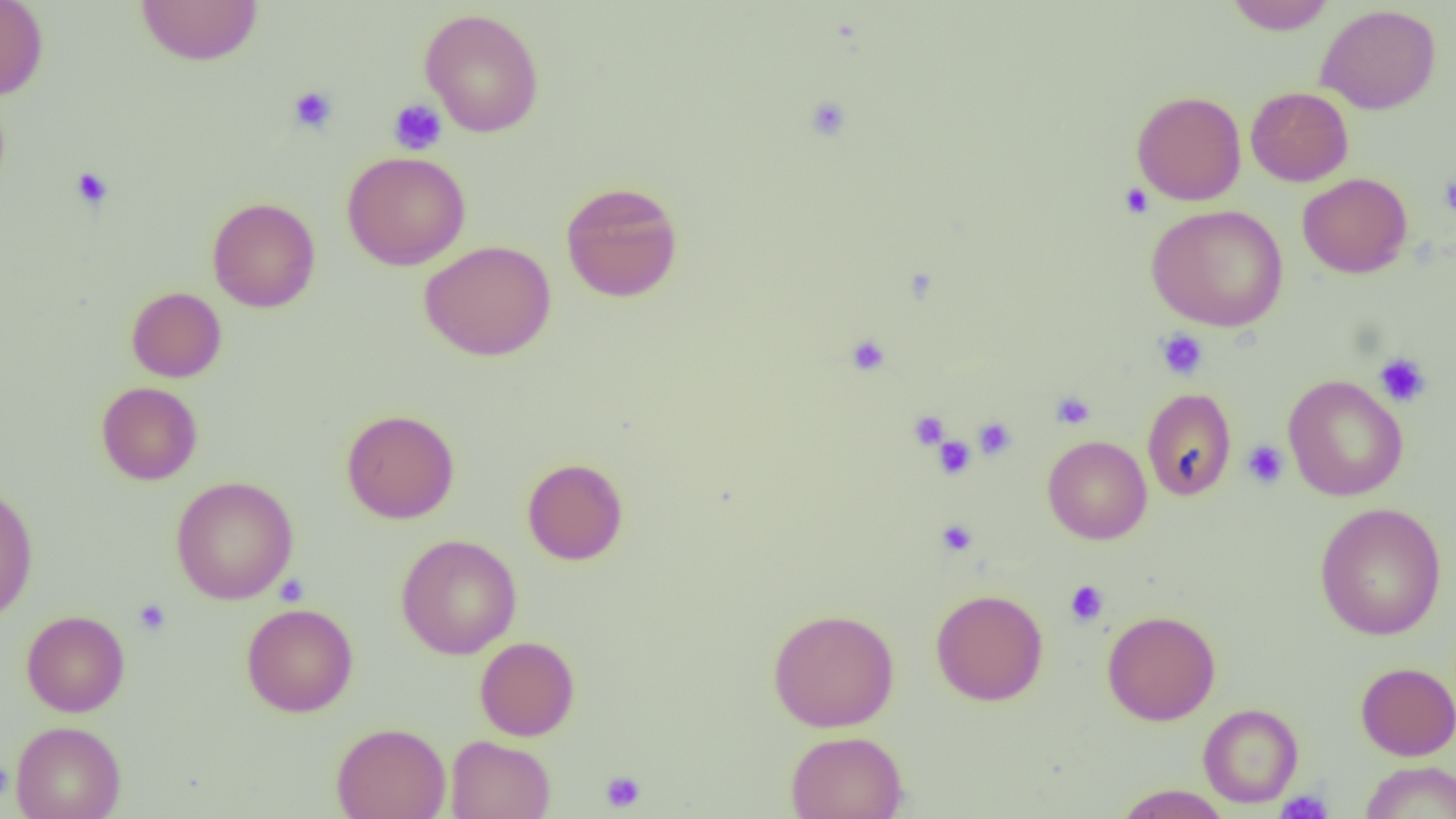

Approximate bounding boxes as (x1,y1)-(x2,y2) corner pairs in pixels. Uninfected red blood cell locations: (0,0)-(49,100), (1225,0)-(1336,34), (136,1)-(263,66), (1316,4)-(1442,114), (419,9)-(544,137), (1245,86)-(1353,186), (1132,90)-(1246,205), (341,151)-(471,270), (1298,173)-(1412,278), (560,181)-(684,303), (207,197)-(320,313), (1147,204)-(1288,331), (419,240)-(556,361), (126,287)-(227,382), (1283,374)-(1408,501), (96,382)-(202,485), (1142,388)-(1236,501), (341,408)-(459,524), (1042,435)-(1152,544), (522,457)-(629,565), (171,476)-(298,604), (0,484)-(38,622), (1314,503)-(1447,640), (396,534)-(522,659), (930,588)-(1049,705), (241,602)-(358,717), (768,608)-(900,732), (21,610)-(130,716), (1102,610)-(1220,725), (475,636)-(580,741), (1356,662)-(1456,760), (1198,703)-(1303,808), (10,721)-(126,819), (331,722)-(450,819), (785,730)-(908,819), (445,735)-(556,819), (1360,760)-(1456,818), (1113,784)-(1232,818). Platelet locations: (288,85)-(338,134), (804,96)-(852,141), (388,98)-(447,156), (70,167)-(114,210), (1438,175)-(1456,217), (1119,182)-(1154,218), (1156,329)-(1209,380), (845,334)-(891,376), (1373,352)-(1432,408), (1051,392)-(1095,430), (909,410)-(949,450), (973,417)-(1017,459), (933,435)-(976,479), (1241,440)-(1289,489), (936,519)-(978,556), (1065,580)-(1109,626), (133,598)-(171,636), (599,771)-(646,813), (1276,789)-(1333,819). Slide-level diagnosis: no evidence of blood parasites. Light microscopy. Thin blood film. Captured at 1000x magnification. One field of a larger specimen. Image is 1456×819 pixels.